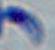
Summary:
  - Identification: Toxoplasma gondii
  - Magnification: 1000x
  - Modality: micrograph